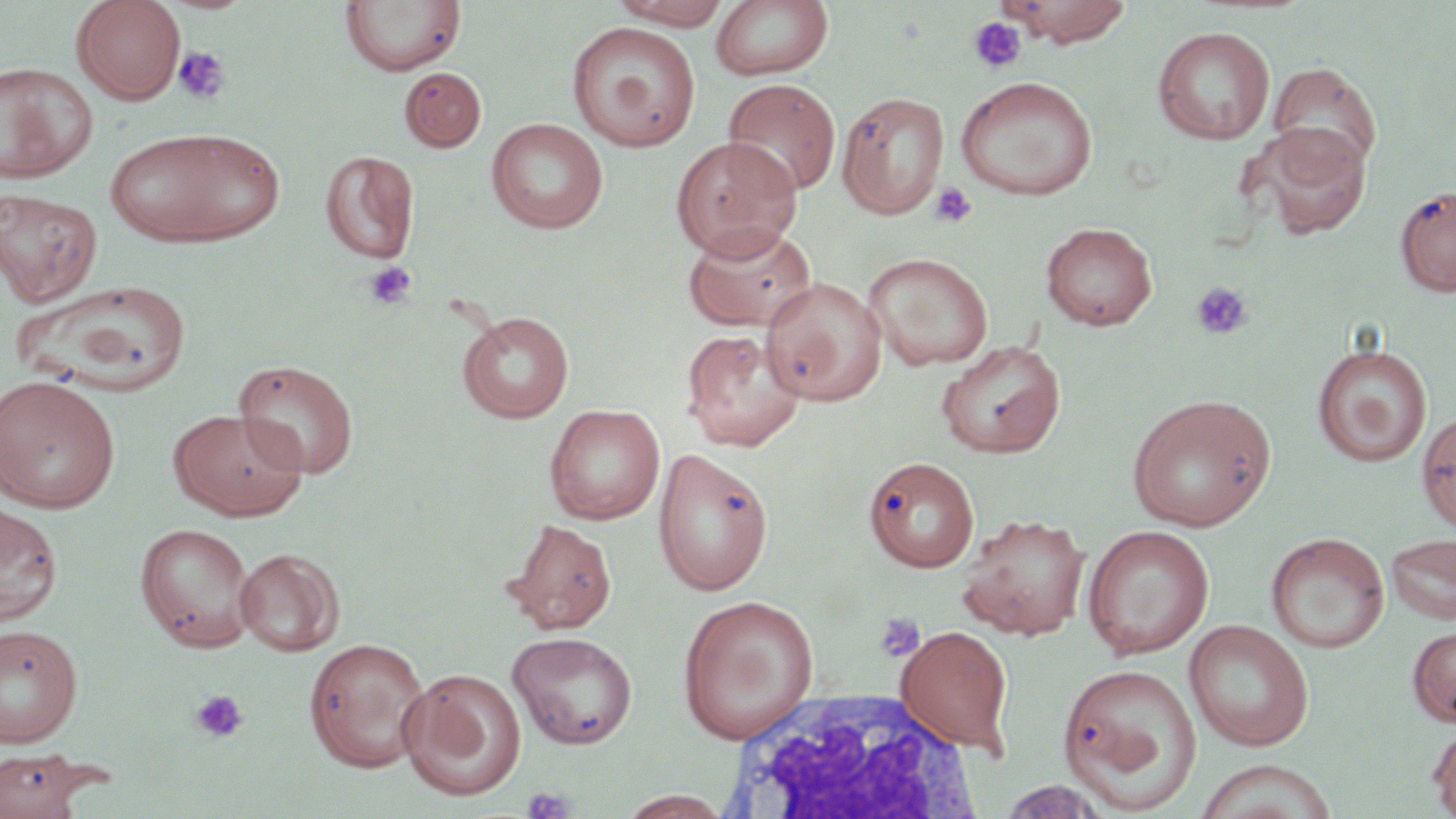

Approximate bounding boxes as (x1, y1, x2, y2) in pixels. Uninfected red blood cell locations: (71, 0, 186, 104), (609, 0, 733, 29), (995, 0, 1134, 46), (340, 1, 466, 76), (710, 1, 834, 82), (568, 22, 702, 151), (1152, 25, 1276, 145), (0, 62, 99, 183), (1268, 62, 1382, 177), (399, 67, 486, 152), (955, 76, 1098, 200), (722, 78, 841, 198), (838, 91, 948, 219), (486, 118, 609, 234), (1245, 123, 1374, 240), (104, 127, 285, 248), (669, 135, 802, 260), (319, 150, 420, 265), (1395, 184, 1456, 297), (1, 189, 103, 307), (682, 222, 819, 333), (1041, 222, 1158, 330), (863, 252, 993, 371), (761, 277, 887, 407), (14, 278, 192, 397), (457, 310, 574, 423), (680, 328, 805, 451), (936, 339, 1065, 458), (1313, 344, 1432, 468), (233, 358, 359, 478), (0, 375, 120, 512), (1126, 393, 1277, 532), (544, 404, 665, 524), (167, 408, 308, 521), (1416, 409, 1456, 536), (653, 446, 774, 596), (863, 455, 980, 573), (0, 501, 64, 626), (957, 514, 1090, 639), (504, 518, 617, 635), (135, 522, 258, 652), (1082, 525, 1215, 659), (1267, 532, 1390, 653), (1385, 532, 1456, 626), (234, 548, 345, 656), (678, 594, 819, 743), (1184, 619, 1315, 751), (1408, 624, 1456, 727), (0, 625, 82, 748), (895, 625, 1014, 753), (507, 631, 638, 750), (304, 636, 431, 773), (1057, 662, 1202, 812), (398, 668, 527, 802), (1427, 722, 1456, 819), (0, 749, 88, 818), (1192, 759, 1339, 818), (998, 779, 1111, 818), (615, 790, 735, 818). White blood cell locations: (720, 688, 986, 818). Platelet locations: (968, 16, 1027, 74), (172, 45, 230, 105), (930, 182, 978, 228), (363, 261, 418, 311), (1191, 281, 1254, 341), (874, 613, 925, 662), (189, 689, 249, 744), (520, 786, 575, 819). Slide-level diagnosis: no evidence of blood parasites. One field of a larger specimen. Thin blood smear. Light microscopy. 1000x magnification. Image is 1456×819 pixels. May-Grünwald-Giemsa stain.